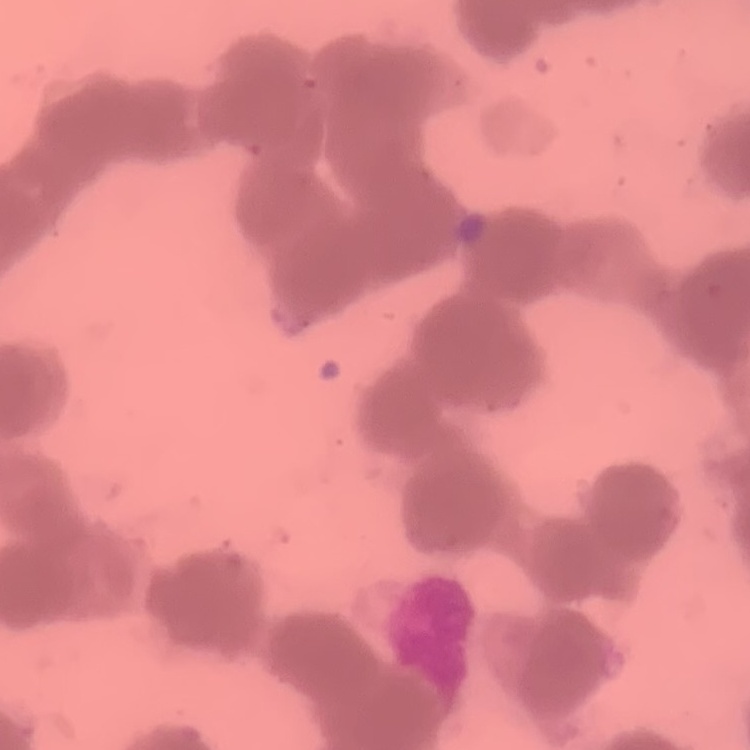
red blood cell morphology = rouleaux formation
image type = one tile cut from a larger photomicrograph
preparation = thin blood film
stain = Field's or Giemsa